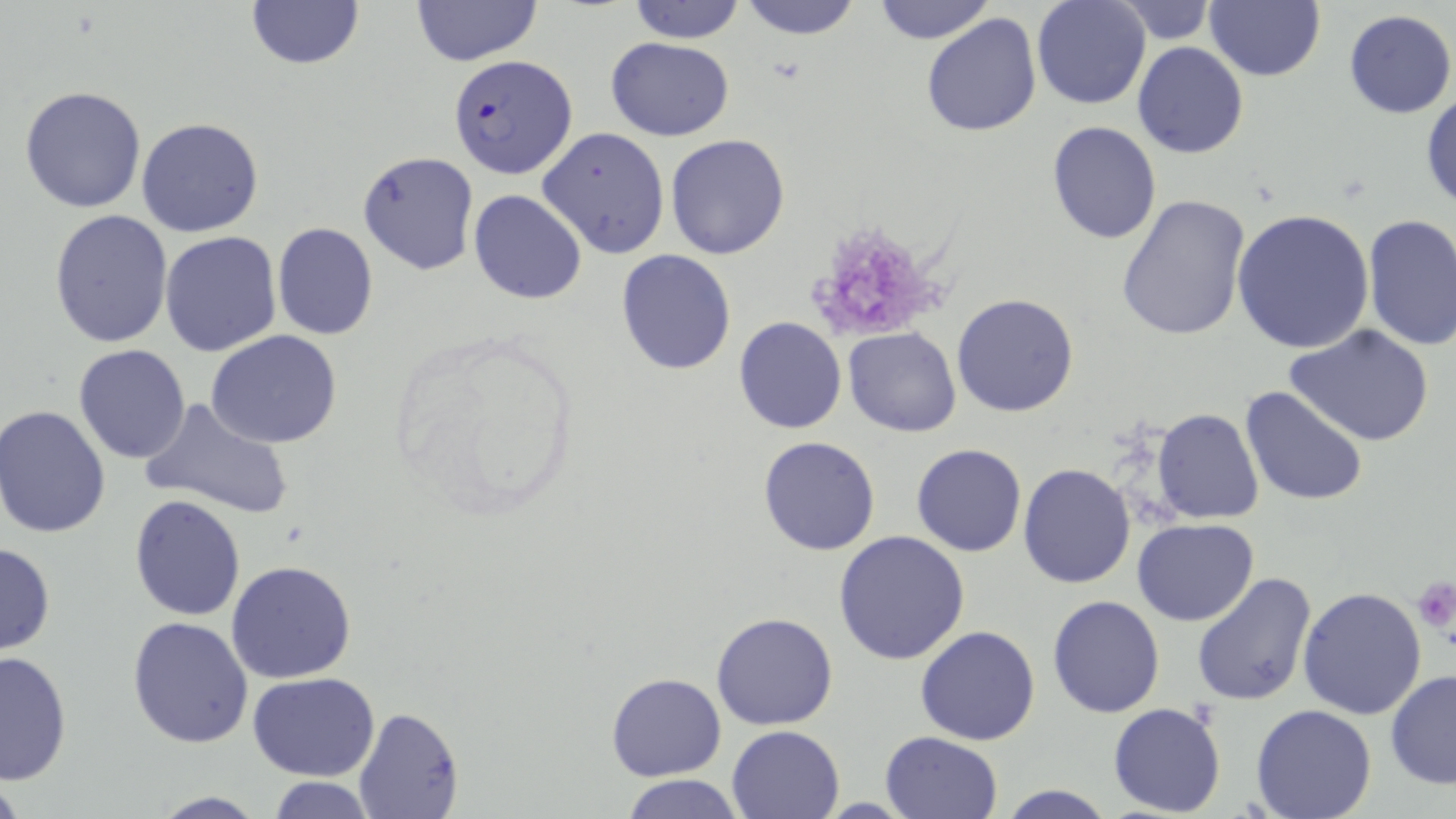
Approximate bounding boxes as named x1/y1/x2/y2 corners in pixels. Plasmodium falciparum-infected red blood cell locations: (x1=452, y1=55, x2=582, y2=181). Uninfected red blood cell locations: (x1=243, y1=0, x2=366, y2=72), (x1=410, y1=0, x2=543, y2=67), (x1=627, y1=0, x2=747, y2=44), (x1=736, y1=0, x2=863, y2=41), (x1=1031, y1=0, x2=1150, y2=110), (x1=1116, y1=0, x2=1215, y2=45), (x1=1206, y1=0, x2=1324, y2=82), (x1=869, y1=1, x2=997, y2=44), (x1=1344, y1=9, x2=1456, y2=119), (x1=921, y1=12, x2=1040, y2=137), (x1=606, y1=36, x2=733, y2=140), (x1=1132, y1=42, x2=1248, y2=160), (x1=20, y1=86, x2=147, y2=213), (x1=1421, y1=90, x2=1455, y2=214), (x1=137, y1=118, x2=265, y2=238), (x1=1047, y1=122, x2=1161, y2=244), (x1=538, y1=127, x2=670, y2=257), (x1=665, y1=133, x2=791, y2=259), (x1=482, y1=151, x2=651, y2=285), (x1=357, y1=152, x2=479, y2=276), (x1=469, y1=189, x2=588, y2=305), (x1=1117, y1=194, x2=1251, y2=342), (x1=49, y1=209, x2=173, y2=348), (x1=1233, y1=209, x2=1374, y2=353), (x1=1361, y1=215, x2=1456, y2=352), (x1=272, y1=222, x2=378, y2=341), (x1=159, y1=231, x2=283, y2=358), (x1=615, y1=249, x2=738, y2=375), (x1=951, y1=293, x2=1079, y2=416), (x1=734, y1=317, x2=847, y2=436), (x1=1284, y1=322, x2=1436, y2=448), (x1=843, y1=327, x2=961, y2=437), (x1=207, y1=329, x2=343, y2=449), (x1=72, y1=344, x2=192, y2=464), (x1=1240, y1=385, x2=1368, y2=508), (x1=139, y1=398, x2=296, y2=522), (x1=1, y1=405, x2=115, y2=540), (x1=1153, y1=408, x2=1263, y2=524), (x1=757, y1=435, x2=882, y2=556), (x1=911, y1=443, x2=1026, y2=558), (x1=1018, y1=462, x2=1138, y2=588), (x1=129, y1=495, x2=246, y2=621), (x1=1132, y1=518, x2=1259, y2=625), (x1=831, y1=529, x2=972, y2=667), (x1=0, y1=541, x2=55, y2=656), (x1=226, y1=560, x2=357, y2=684), (x1=1191, y1=570, x2=1317, y2=708), (x1=1297, y1=586, x2=1428, y2=721), (x1=1047, y1=595, x2=1164, y2=718), (x1=711, y1=611, x2=839, y2=731), (x1=128, y1=615, x2=254, y2=748), (x1=915, y1=626, x2=1041, y2=745), (x1=0, y1=650, x2=72, y2=785), (x1=1385, y1=669, x2=1456, y2=789), (x1=249, y1=672, x2=380, y2=780), (x1=606, y1=672, x2=725, y2=781), (x1=1108, y1=702, x2=1227, y2=817), (x1=353, y1=704, x2=463, y2=818), (x1=1250, y1=704, x2=1378, y2=819), (x1=726, y1=724, x2=844, y2=818), (x1=880, y1=732, x2=1004, y2=819), (x1=620, y1=774, x2=746, y2=818), (x1=264, y1=777, x2=379, y2=817), (x1=994, y1=782, x2=1117, y2=819), (x1=149, y1=792, x2=270, y2=818). Platelet locations: (x1=811, y1=228, x2=948, y2=335), (x1=1411, y1=576, x2=1456, y2=630). Slide-level diagnosis: Plasmodium falciparum. Optical microscopy. Thin blood smear. May-Grünwald-Giemsa stain. One field of a larger specimen. Image is 1456×819 pixels. 1000x magnification.